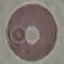

Summary:
  - Result: no malaria parasites seen
  - Stain: Giemsa
  - Capture: smartphone through the microscope eyepiece
  - Preparation: thin blood film
  - Image type: automatically extracted cell patch, resized to 64 × 64 pixels